Classify this cell by malaria status.
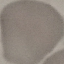

It is uninfected.

Summary:
  - Capture: smartphone camera at the microscope eyepiece
  - Image type: automatically extracted cell patch, resized to 64 × 64 pixels
  - Preparation: thin blood film
  - Stain: Giemsa